Report the malaria status.
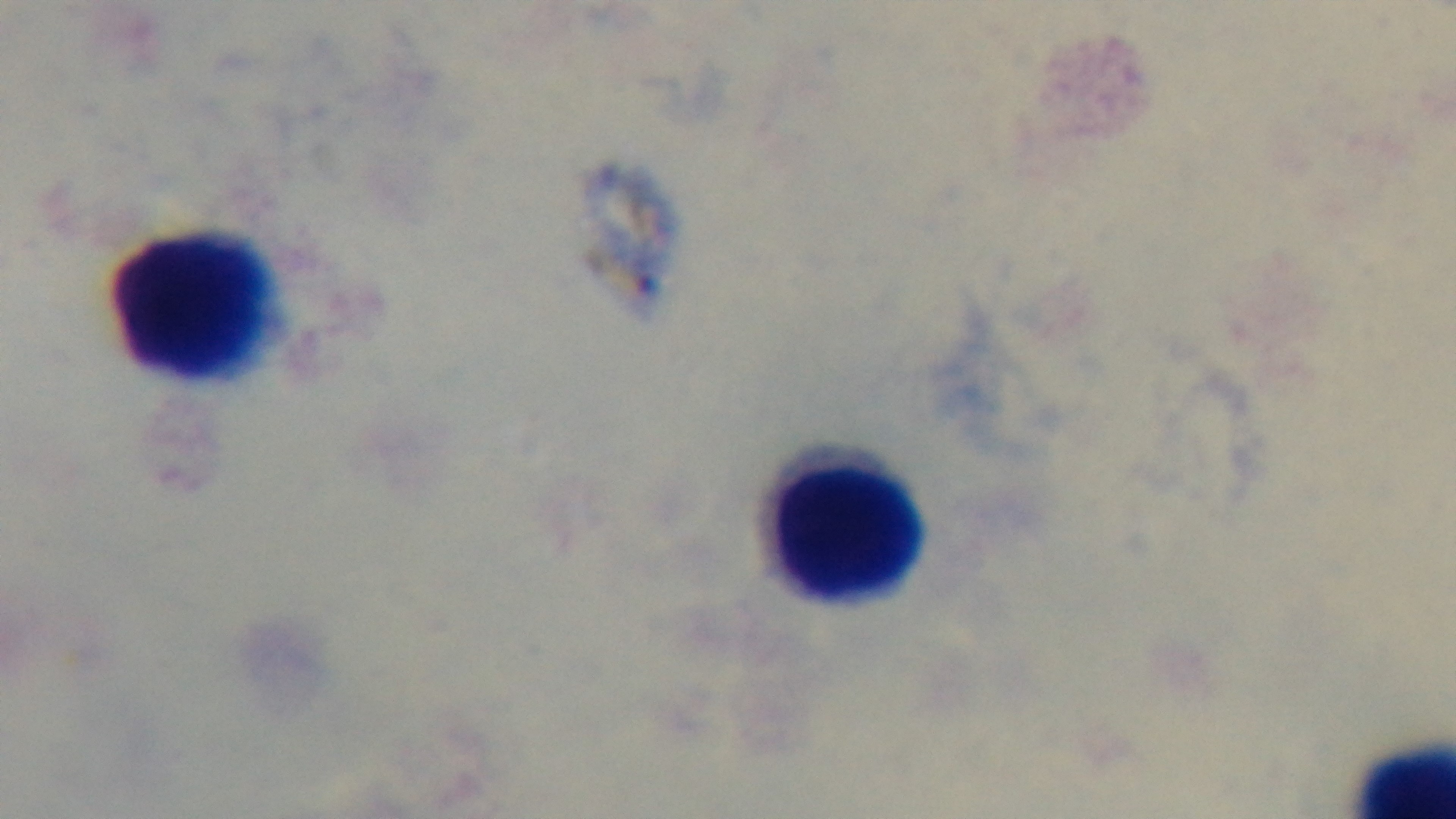
Uninfected.

field of view = one from the slide
modality = light microscopy
stain = Giemsa
objective = 100x oil immersion
capture = mounted 4K digital camera
preparation = thick blood film